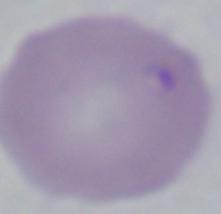
Micrograph. A Babesia parasite is shown. 1000x magnification.